Name the parasite shown.
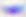

Toxoplasma gondii.

Micrograph. Captured at 400x magnification.